Classify this cell by malaria status.
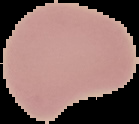
Uninfected.

Summary:
  - Preparation: thin blood film
  - Image size: 139×124 pixels
  - Image type: segmented cell region on a black background